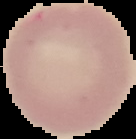

Summary:
  - Malaria status: uninfected
  - Image size: 136×139 pixels
  - Image type: segmented cell region on a black background
  - Preparation: thin blood film